Evaluate for Plasmodium parasites.
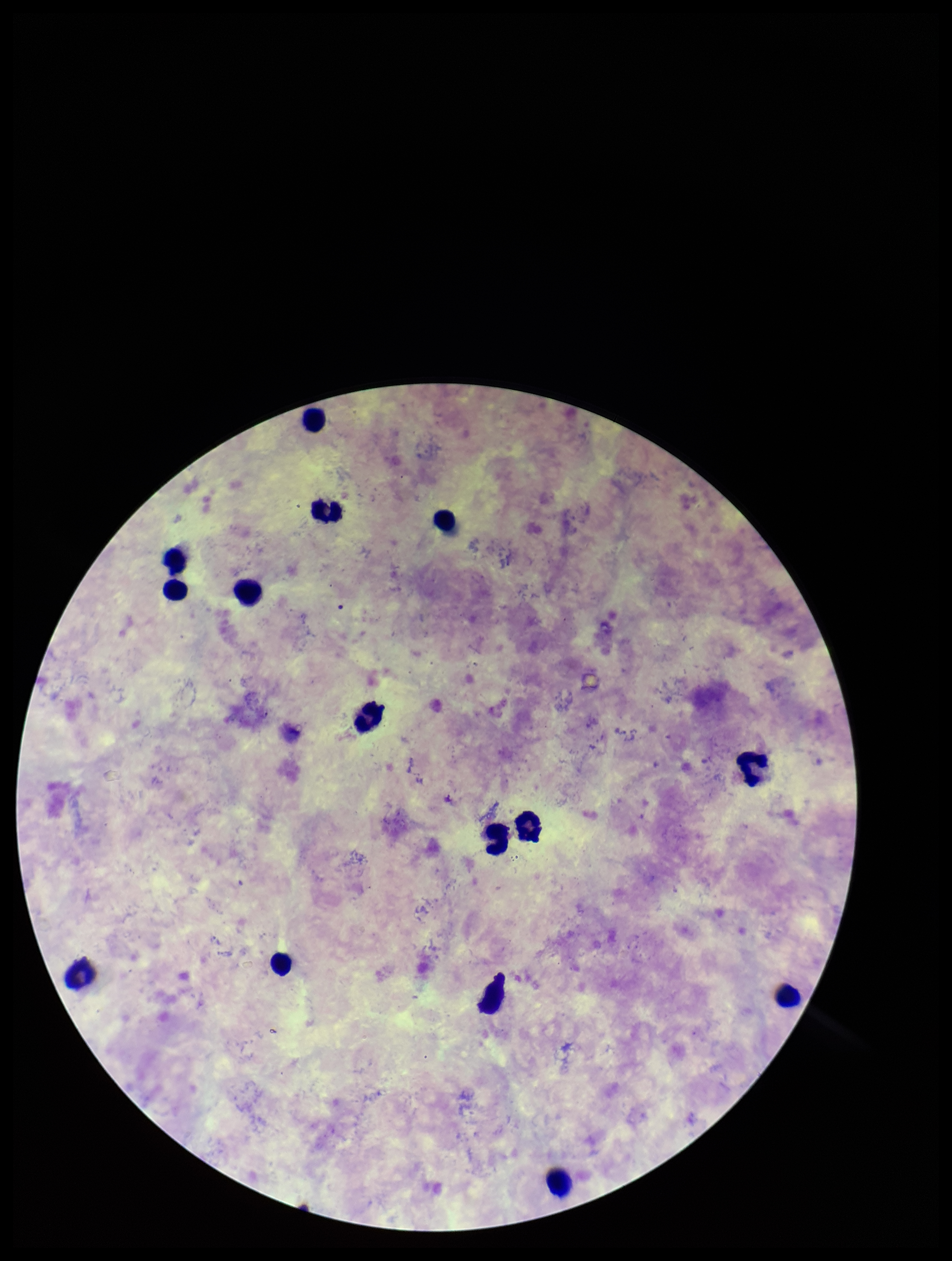
None identified.

Summary:
  - Leukocyte count: 15
  - Field of view: one from this slide
  - Capture: smartphone photograph through the microscope eyepiece
  - Preparation: thick blood smear
  - Stain: Giemsa
  - Image size: 952×1261 pixels
  - Species reported for this patient: Plasmodium vivax
  - Parasite count: 0
  - Patient malaria status: infected